Describe the morphology of the red blood cells.
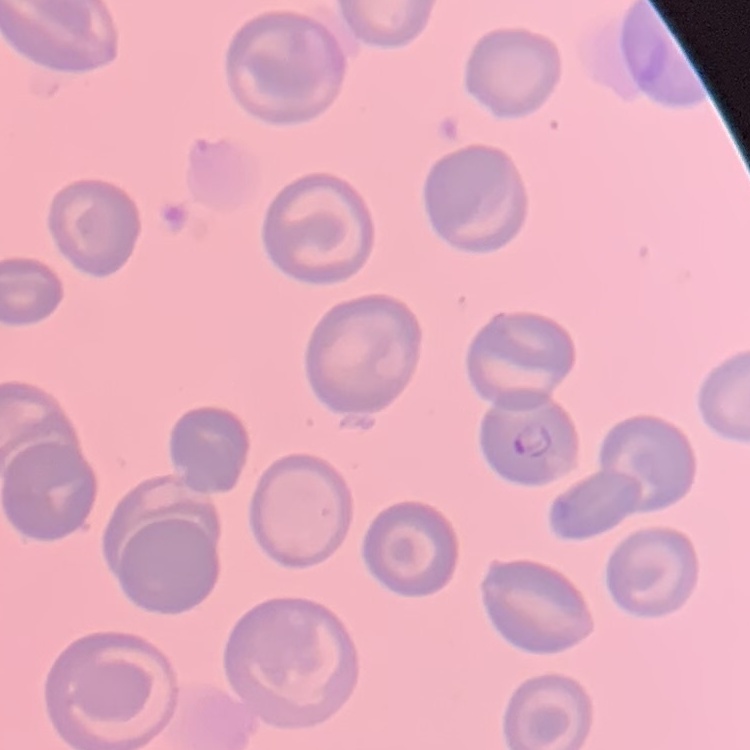

They show no rouleaux formation.

Field's or Giemsa stain. Square crop of a larger photomicrograph. Thin blood film.